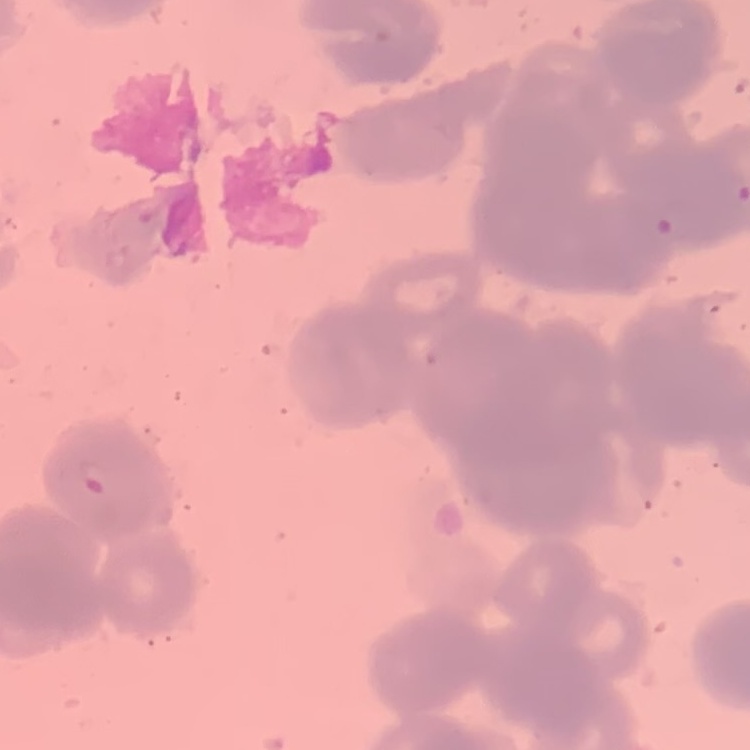

red blood cell morphology = rouleaux formation
image type = one tile cut from a larger photomicrograph
preparation = thin peripheral smear
stain = Field's or Giemsa